Give the preparation type.
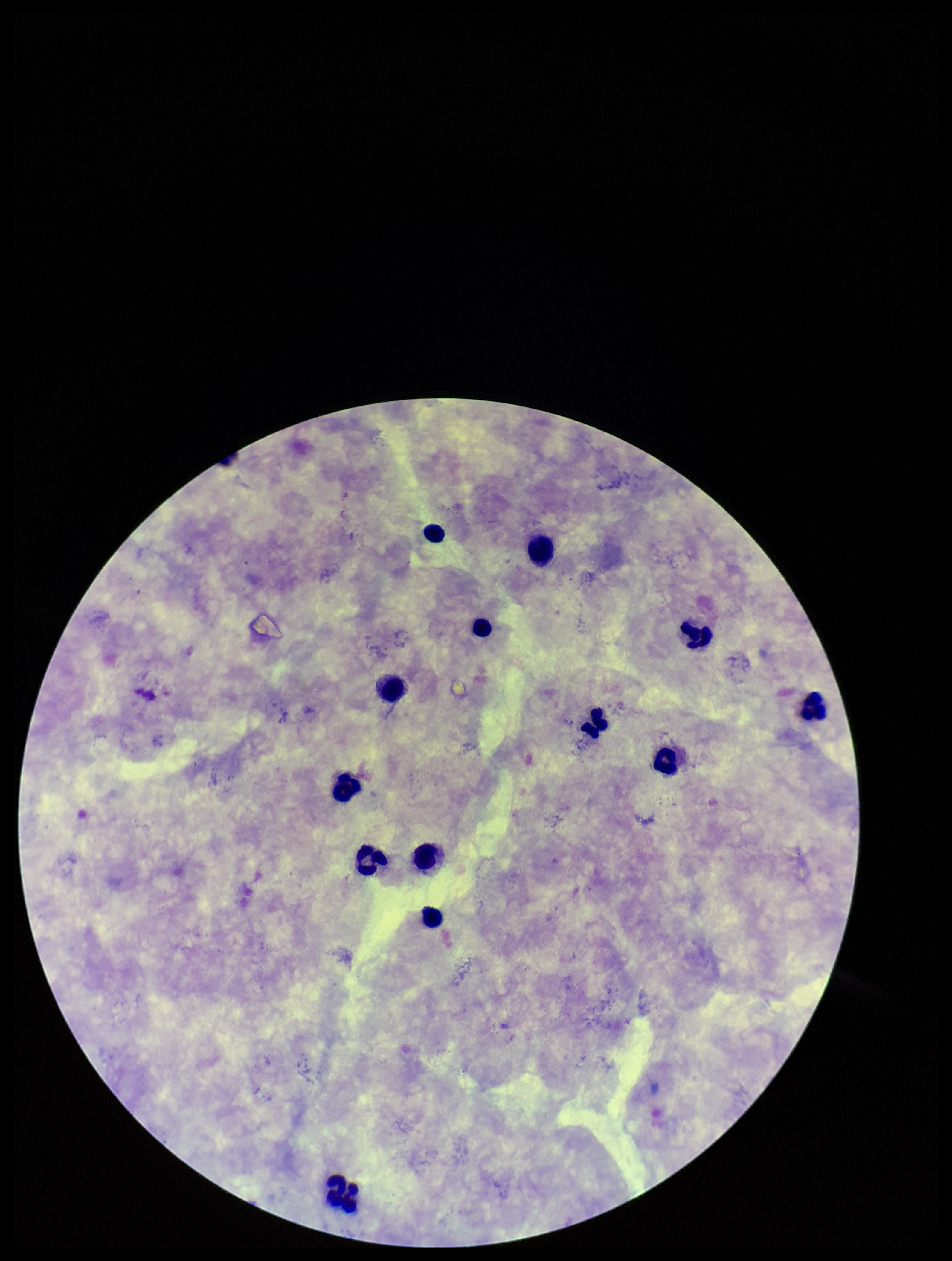
A thick smear.

Leukocyte count: 13. Stained with Giemsa. Plasmodium parasites: none identified. Photographed through the microscope eyepiece with a smartphone camera. Parasite count: 0. Patient malaria status: negative. Image is 952×1261 pixels. One field from this slide.